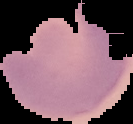
Summary:
  - Image type: segmented cell region with the area outside set to black
  - Result: Plasmodium parasites detected
  - Preparation: thin blood smear
  - Image size: 133×124 pixels